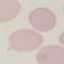
Summary:
  - Malaria status: uninfected
  - Image type: automatically extracted cell patch, resized to 64 × 64 pixels
  - Preparation: thin smear
  - Capture: smartphone through the microscope eyepiece
  - Stain: Giemsa